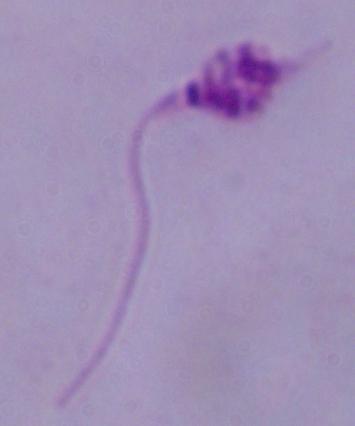
identification = Leishmania
modality = micrograph
magnification = 1000x